Describe the morphology of the erythrocytes.
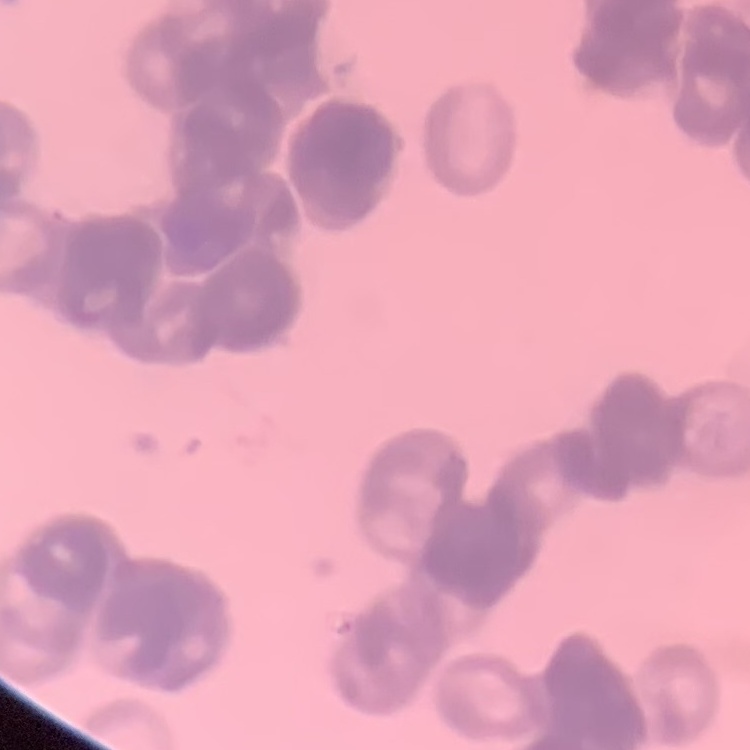

Rouleaux formation.

Summary:
  - Preparation: thin blood film
  - Image type: square crop of a larger photomicrograph
  - Stain: Field's or Giemsa